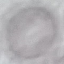

Summary:
  - Result: no malaria parasites seen
  - Stain: Giemsa
  - Image type: automatically extracted cell patch, resized to 64 × 64 pixels
  - Preparation: thin blood smear
  - Capture: smartphone camera at the microscope eyepiece